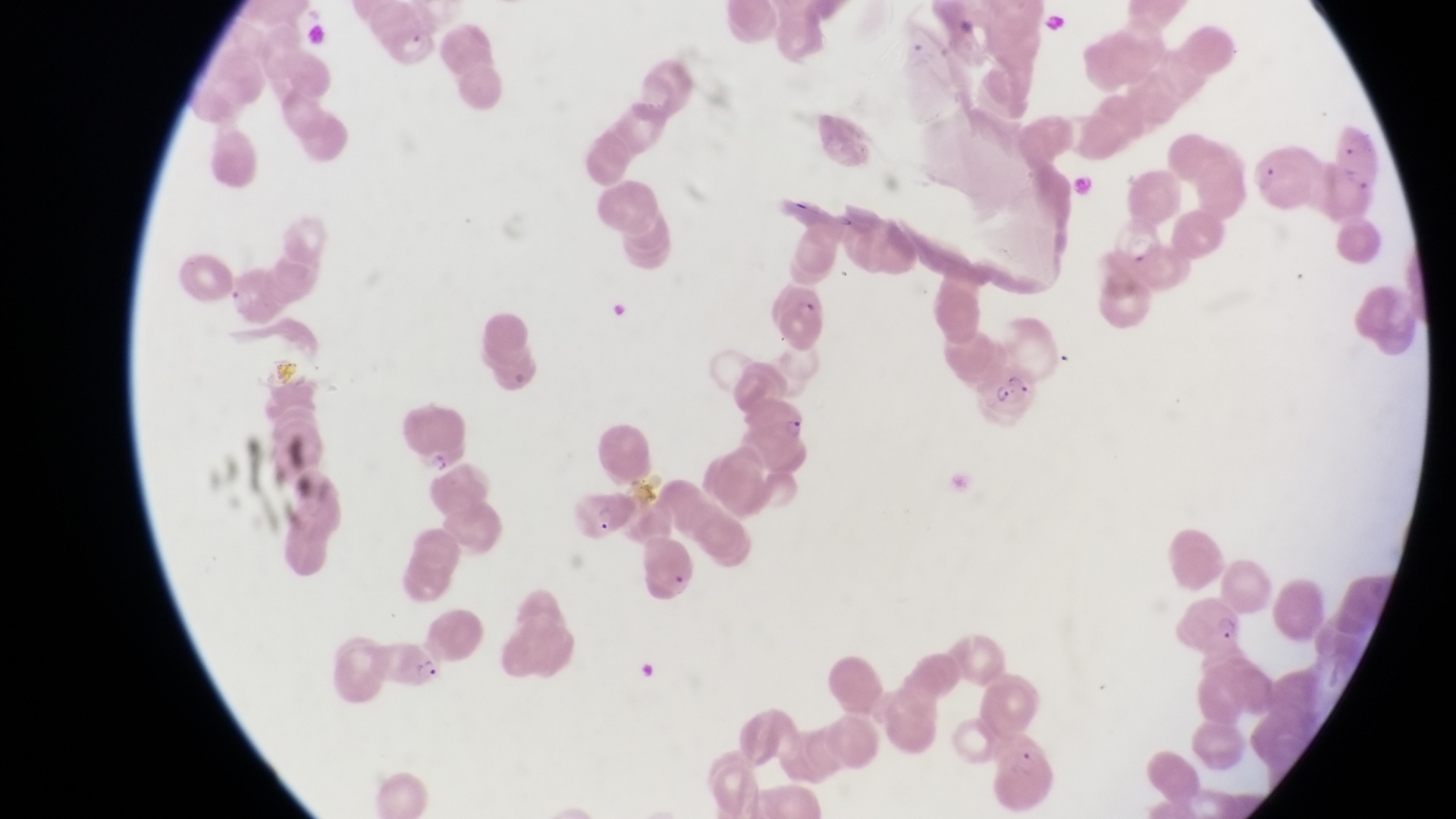

Approximate bounding boxes as {left, top, right, bottom} in pixels.
Summary:
  - Parasitised red blood cell locations: {383, 19, 442, 71}, {1329, 112, 1387, 215}, {1254, 149, 1323, 215}, {1110, 211, 1171, 272}, {769, 275, 827, 352}, {981, 353, 1039, 432}, {397, 394, 469, 473}, {755, 396, 818, 462}, {568, 486, 635, 544}, {637, 529, 706, 611}, {383, 634, 446, 692}
  - Artifact (platelet-like body, stain precipitate, or debris) locations: {1043, 8, 1070, 41}
  - Field of view: single
  - Magnification: 1000x
  - Preparation: thin blood smear
  - Image size: 1456×819 pixels
  - Capture: smartphone photograph through the eyepiece of an Olympus CX-23 microscope
  - Country: Uganda